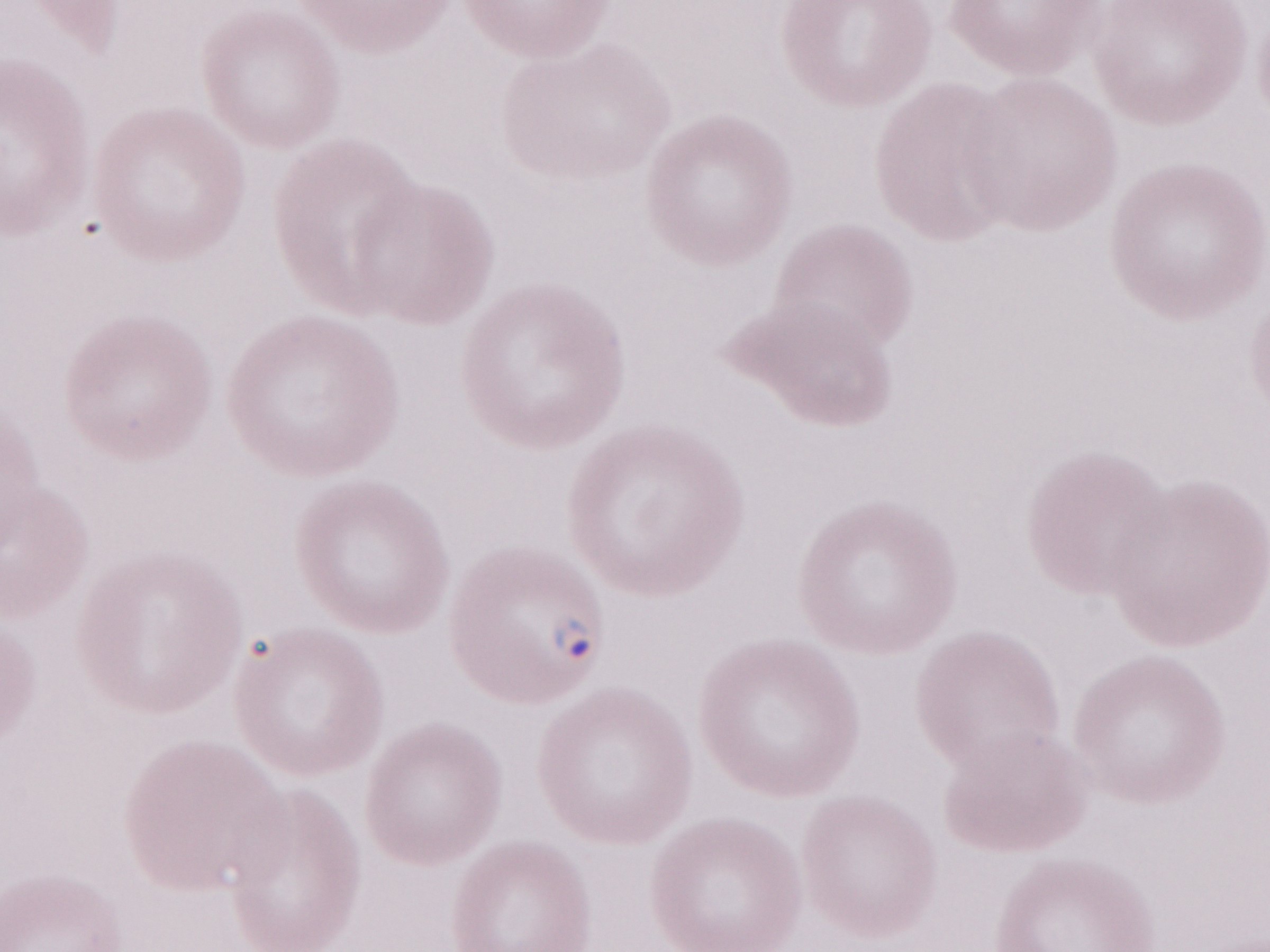

Thin peripheral-blood smear. Image is 1270×952 pixels. Magnification: 1,000x. Olympus BX43 microscope and DP73 digital camera. One field of this slide. May-Grünwald-Giemsa stain. Malaria diagnosis (patient-level): positive.